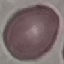
Summary:
  - Result: negative for malaria parasites
  - Preparation: thin blood film
  - Capture: smartphone camera at the microscope eyepiece
  - Image type: automatically extracted cell patch, resized to 64 × 64 pixels
  - Stain: Giemsa